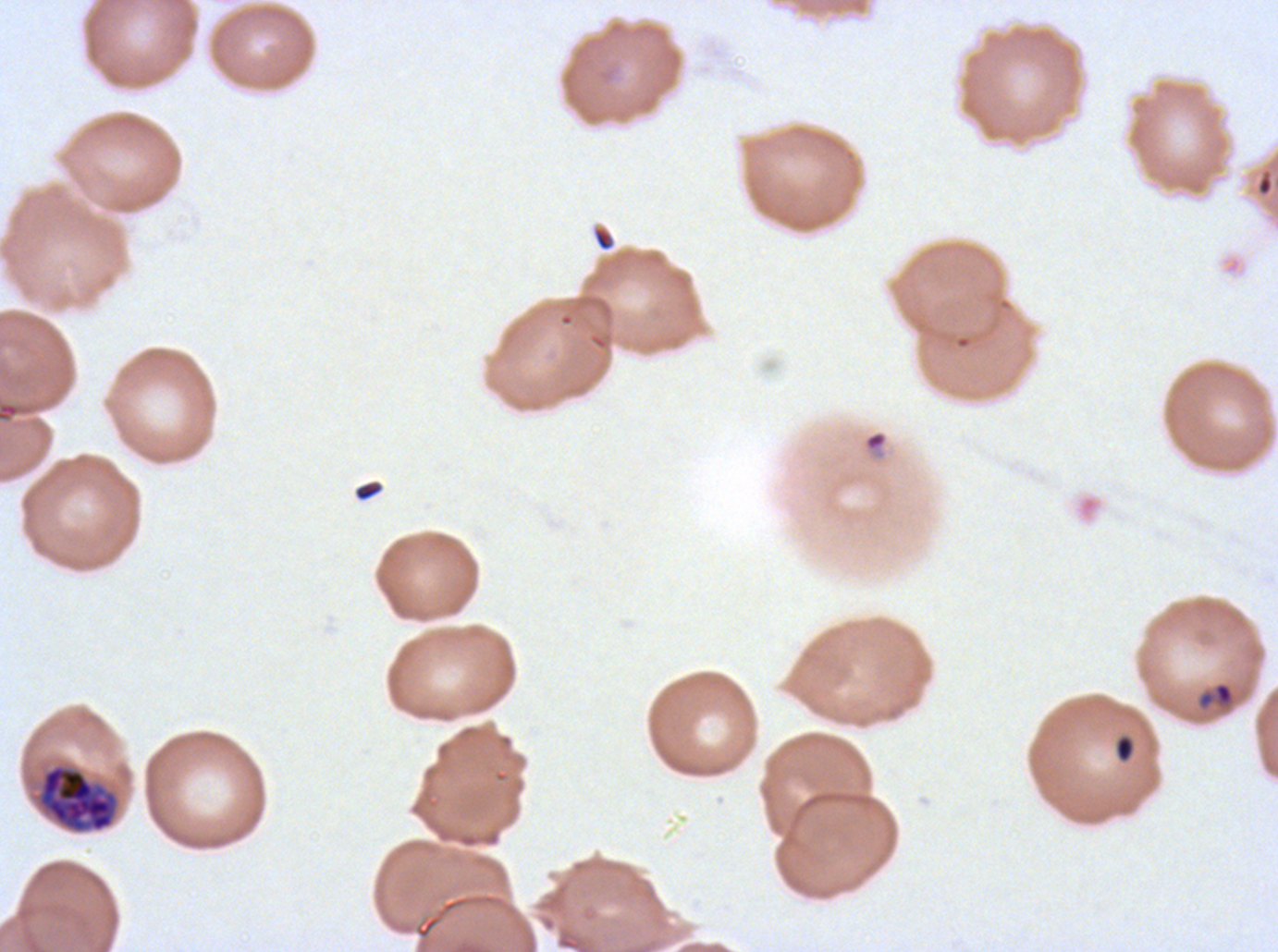 Approximate bounding boxes as [x1, y1, x2, y2] in pixels. Ring locations: [864, 430, 888, 452]. Early schizont locations: [37, 763, 119, 834]. Late-ring/early-trophozoite locations: [1196, 680, 1236, 712]. Debris locations: [591, 226, 616, 252], [353, 480, 384, 502], [1113, 733, 1137, 764]. Thin blood film. P. falciparum cultured ex vivo for 24 to 48 hours, from a patient in The Gambia. Image is 1278×952 pixels. Giemsa-stained preparation. A sub-image separated from a larger composite. Life-cycle stages observed: ring, late-ring/early-trophozoite, early schizont.